State which cell type is depicted.
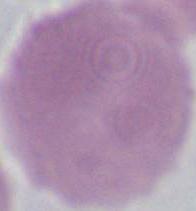

This is an erythrocyte.

Summary:
  - Magnification: 1000x
  - Modality: photomicrograph